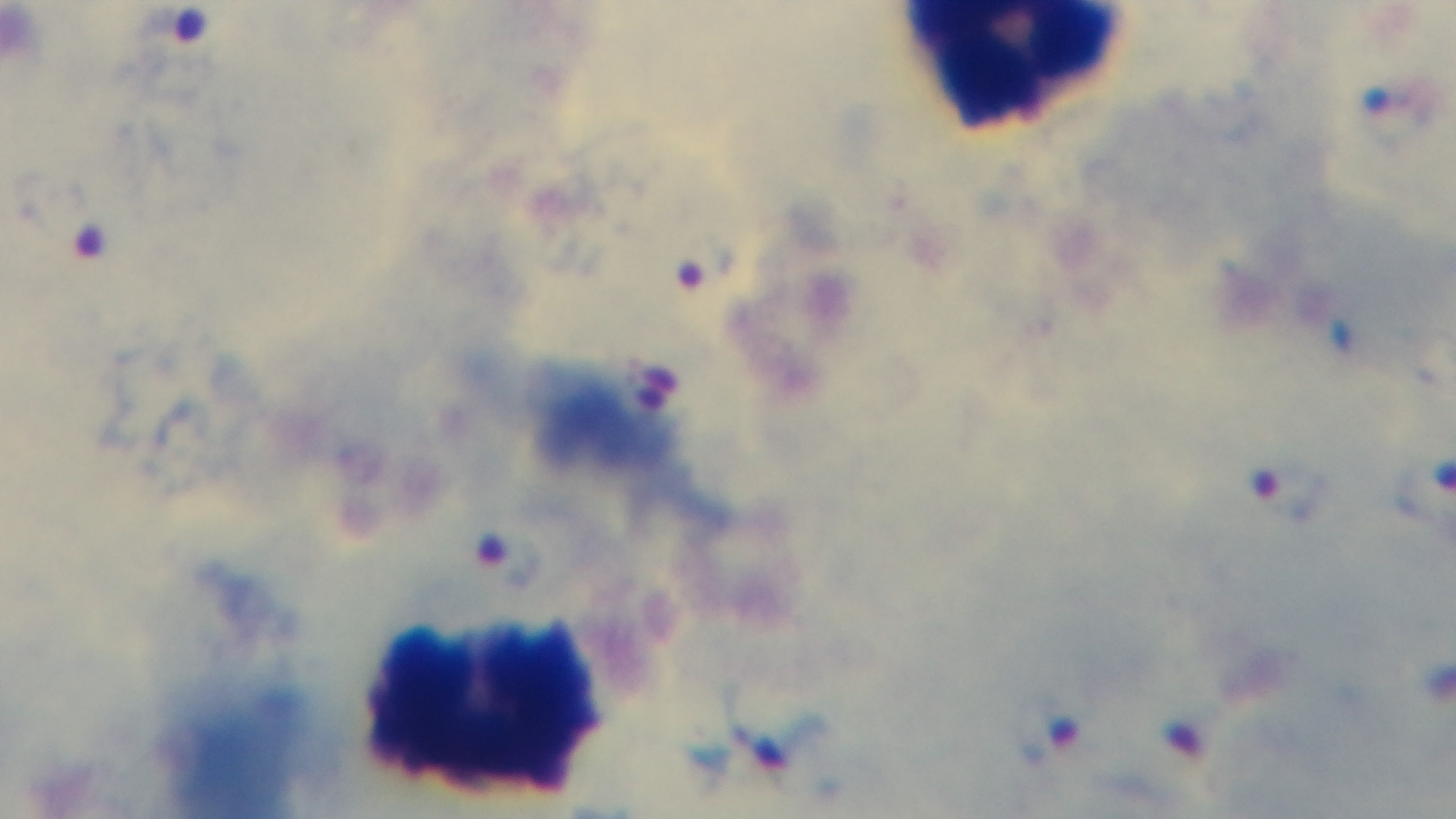 100x oil-immersion objective. Light microscopy. Giemsa-stained. Malaria status: positive. Mounted 4K digital camera. One field from the slide. Preparation: thick blood film.